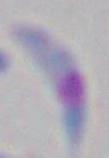

Toxoplasma gondii is seen. 1000x magnification. Micrograph.